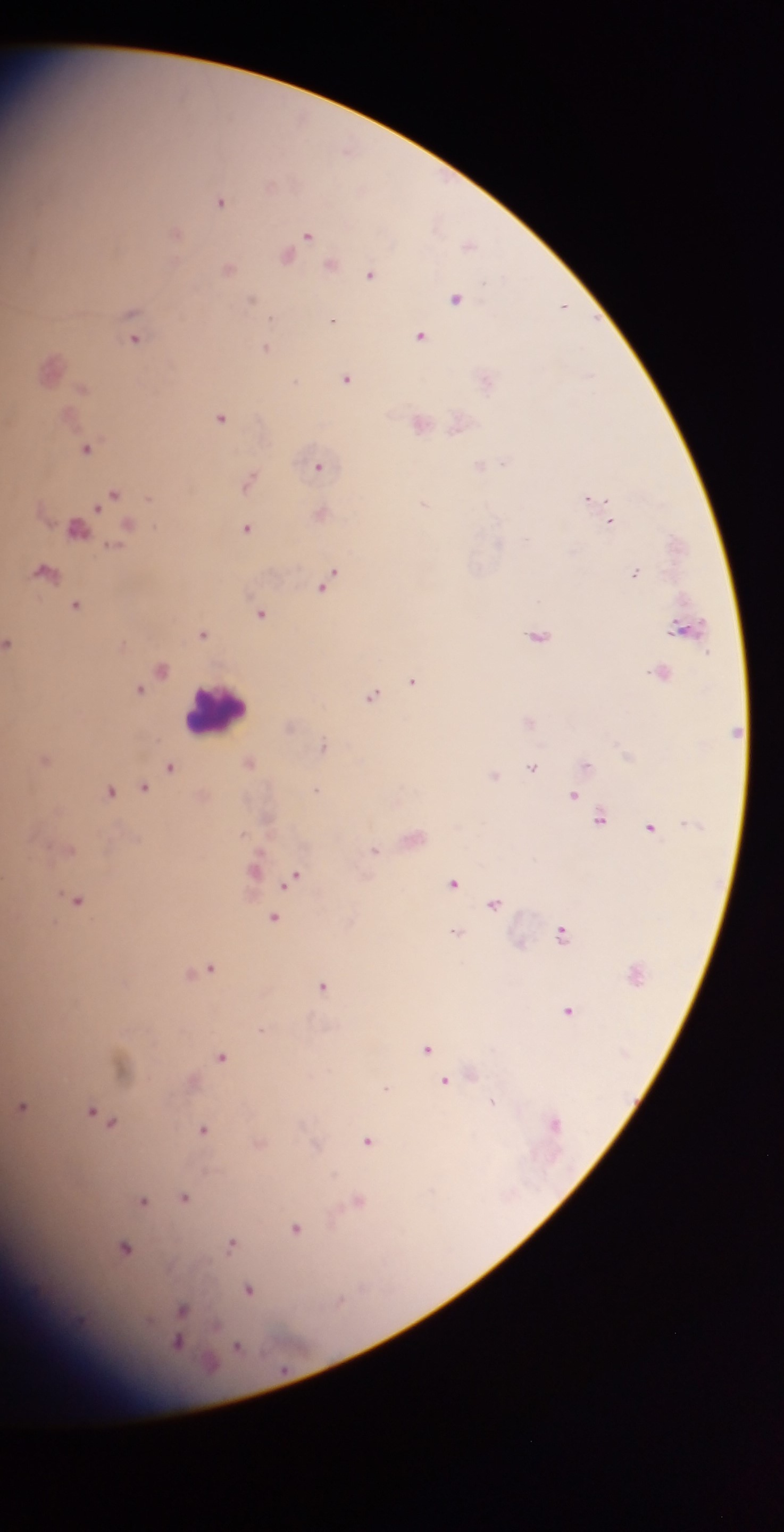
Approximate centers as [x, y] in pixels.
Summary:
  - Malaria parasite locations: [271, 185], [221, 199], [176, 231], [308, 235], [470, 243], [290, 253], [332, 264], [229, 267], [371, 273], [456, 297], [563, 306], [133, 322], [135, 335], [422, 335], [267, 348], [50, 366], [348, 376], [487, 378], [221, 416], [420, 422], [460, 422], [87, 447], [484, 464], [320, 465], [249, 478], [114, 494], [593, 499], [321, 513], [611, 519], [127, 525], [80, 527], [248, 528], [46, 570], [636, 571], [328, 581], [78, 605], [262, 612], [688, 628], [204, 632], [540, 635], [11, 643], [162, 667], [662, 671], [414, 680], [140, 689], [373, 695], [530, 721], [290, 726], [325, 746], [45, 758], [251, 760], [588, 764], [170, 765], [533, 767], [494, 775], [144, 788], [110, 789], [319, 790], [576, 796], [602, 817], [652, 826], [414, 837], [375, 850], [255, 868], [295, 876], [455, 882], [78, 899], [496, 901], [275, 917], [564, 932], [458, 933], [205, 968], [324, 985], [569, 1009], [264, 1030], [427, 1047], [223, 1056], [122, 1063], [472, 1073], [193, 1080], [445, 1081], [386, 1088], [492, 1104], [23, 1105], [104, 1117], [205, 1129], [370, 1140], [260, 1143], [185, 1196], [144, 1200], [358, 1200], [297, 1228], [233, 1242], [125, 1248], [250, 1289], [182, 1309], [180, 1338], [237, 1346]
  - Leukocyte locations: [215, 709]
  - Image size: 784×1532 pixels
  - Preparation: thick blood smear
  - Capture: mobile-phone photograph through a microscope
  - Country: Ghana
  - Field of view: single